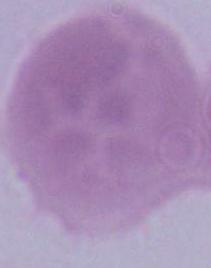
magnification: 1000x
modality: photomicrograph
identification: red blood cell